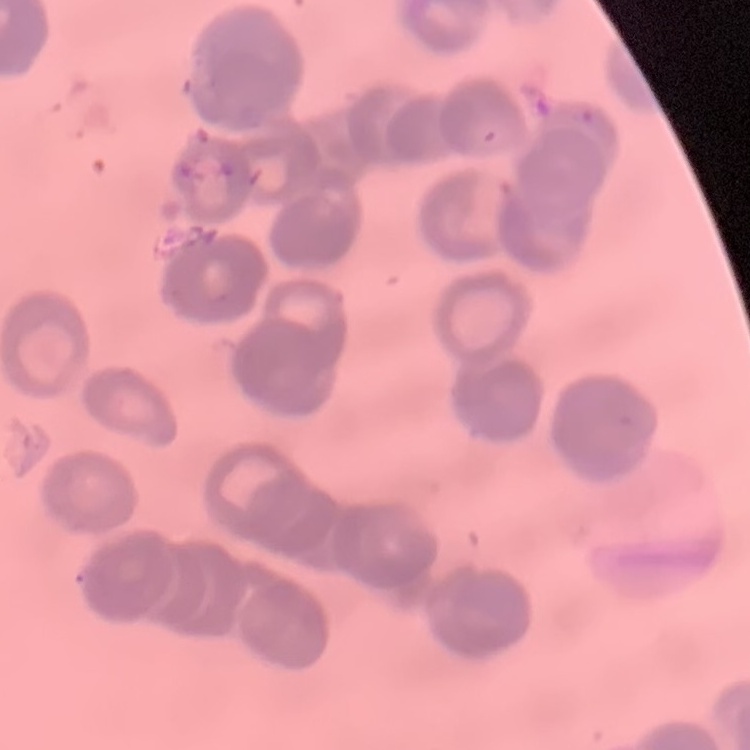 The erythrocytes exhibit rouleaux formation. One tile cut from a larger photomicrograph. Stained with either Field's or Giemsa. Thin blood film.